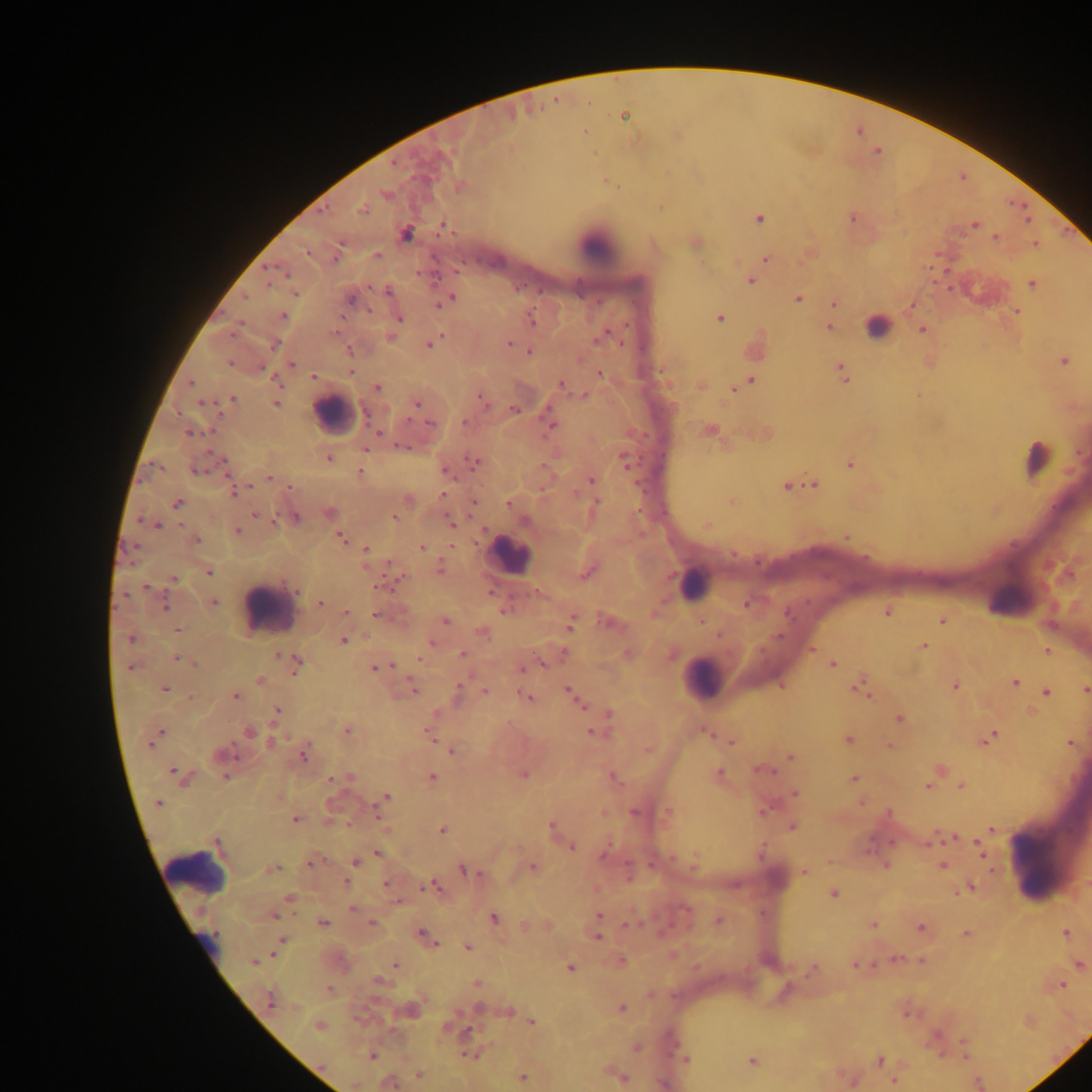

{
  "preparation": "thick blood smear",
  "field_of_view": "single",
  "plasmodium_parasite_locations": "approximate centers as {x, y} in pixels: {624, 115}, {584, 132}, {605, 181}, {459, 186}, {386, 194}, {362, 208}, {758, 218}, {852, 218}, {975, 224}, {442, 225}, {406, 233}, {995, 237}, {694, 241}, {1034, 244}, {308, 251}, {810, 253}, {376, 255}, {765, 260}, {749, 280}, {1032, 283}, {389, 291}, {295, 293}, {350, 296}, {445, 299}, {798, 299}, {834, 303}, {911, 305}, {1016, 311}, {283, 316}, {719, 317}, {398, 318}, {531, 319}, {828, 326}, {921, 329}, {390, 336}, {602, 336}, {430, 342}, {510, 342}, {755, 349}, {349, 350}, {529, 352}, {1062, 360}, {292, 364}, {350, 371}, {843, 372}, {600, 374}, {313, 377}, {750, 380}, {190, 383}, {561, 384}, {700, 385}, {740, 385}, {377, 387}, {585, 394}, {918, 394}, {231, 399}, {483, 399}, {275, 403}, {417, 403}, {514, 409}, {464, 421}, {431, 424}, {550, 425}, {709, 430}, {189, 433}, {764, 434}, {328, 457}, {624, 459}, {473, 462}, {849, 464}, {445, 470}, {360, 472}, {269, 478}, {590, 480}, {811, 483}, {786, 485}, {235, 491}, {443, 494}, {407, 500}, {731, 501}, {473, 502}, {177, 503}, {509, 503}, {594, 506}, {401, 509}, {328, 513}, {255, 515}, {394, 517}, {295, 518}, {334, 521}, {450, 523}, {155, 524}, {707, 524}, {237, 531}, {846, 537}, {340, 538}, {196, 539}, {422, 548}, {366, 550}, {733, 554}, {440, 568}, {208, 572}, {588, 572}, {173, 578}, {212, 601}, {164, 603}, {320, 603}, {747, 603}, {887, 611}, {346, 612}, {378, 614}, {445, 621}, {941, 621}, {570, 622}, {607, 622}, {177, 630}, {483, 632}, {131, 638}, {343, 640}, {432, 641}, {922, 646}, {811, 649}, {1046, 650}, {627, 653}, {670, 653}, {462, 654}, {177, 658}, {542, 663}, {832, 663}, {295, 664}, {132, 667}, {376, 668}, {522, 668}, {259, 680}, {1014, 682}, {955, 685}, {859, 686}, {412, 687}, {164, 688}, {1085, 690}, {459, 691}, {569, 691}, {1045, 691}, {484, 692}, {235, 696}, {526, 697}, {577, 701}, {277, 711}, {1031, 711}, {608, 715}, {899, 717}, {347, 730}, {705, 731}, {249, 732}, {592, 732}, {430, 735}, {154, 737}, {988, 737}, {848, 740}, {271, 741}, {730, 741}, {1069, 741}, {888, 745}, {647, 750}, {451, 751}, {304, 753}, {223, 754}, {789, 756}, {761, 769}, {938, 769}, {178, 775}, {522, 775}, {718, 775}, {225, 776}, {336, 778}, {346, 778}, {432, 778}, {613, 778}, {854, 778}, {928, 786}, {960, 786}, {794, 793}, {385, 796}, {862, 802}, {158, 803}, {378, 807}, {763, 809}, {634, 811}, {667, 812}, {602, 813}, {295, 819}, {791, 826}, {552, 828}, {441, 830}, {991, 830}, {945, 836}, {927, 842}, {977, 845}, {570, 847}, {606, 849}, {378, 853}, {981, 854}, {311, 862}, {355, 862}, {694, 862}, {886, 865}, {942, 865}, {532, 867}, {272, 869}, {992, 870}, {466, 871}, {804, 871}, {347, 881}, {386, 885}, {432, 887}, {968, 888}, {833, 893}, {289, 898}, {353, 908}, {274, 915}, {599, 915}, {493, 917}, {717, 920}, {322, 923}, {372, 924}, {873, 924}, {628, 925}, {526, 926}, {920, 928}, {1065, 932}, {965, 933}, {425, 936}, {596, 937}, {281, 942}, {468, 946}, {897, 959}, {254, 961}, {620, 961}, {920, 961}, {395, 964}, {1078, 964}, {855, 965}, {569, 968}, {812, 969}, {379, 982}, {477, 984}, {1061, 985}, {330, 990}, {271, 999}, {620, 1008}, {410, 1009}, {506, 1011}, {532, 1021}, {319, 1026}, {636, 1047}, {470, 1054}, {371, 1056}, {685, 1058}, {751, 1060}, {879, 1060}, {419, 1074}, {618, 1074}, {523, 1077}, {851, 1081}, {893, 1081}, {389, 1082}",
  "country": "Ghana",
  "image_size": "1092×1092 pixels",
  "capture": "mobile-phone photograph through a microscope",
  "leukocyte_locations": "approximate centers as {x, y} in pixels: {596, 244}, {877, 326}, {335, 413}, {1036, 459}, {510, 555}, {694, 584}, {1008, 599}, {267, 608}, {702, 677}, {1045, 856}, {194, 871}"
}